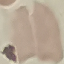 Malaria status: uninfected. Cell patch, automatically extracted from a larger field of view and resized to 64 × 64 pixels. Thin smear of blood. Photographed with a smartphone camera at the microscope eyepiece. Giemsa-stained preparation.